Classify this cell by malaria status.
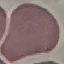
It is uninfected.

Summary:
  - Preparation: thin blood film
  - Stain: Giemsa
  - Image type: cell patch, automatically extracted from a larger field of view and resized to 64 × 64 pixels
  - Capture: smartphone camera at the microscope eyepiece